State which parasite is depicted.
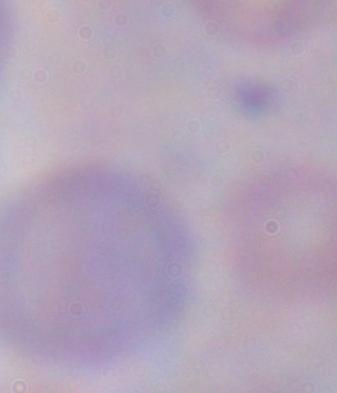
This is a trypanosome.

magnification: 1000x
modality: micrograph